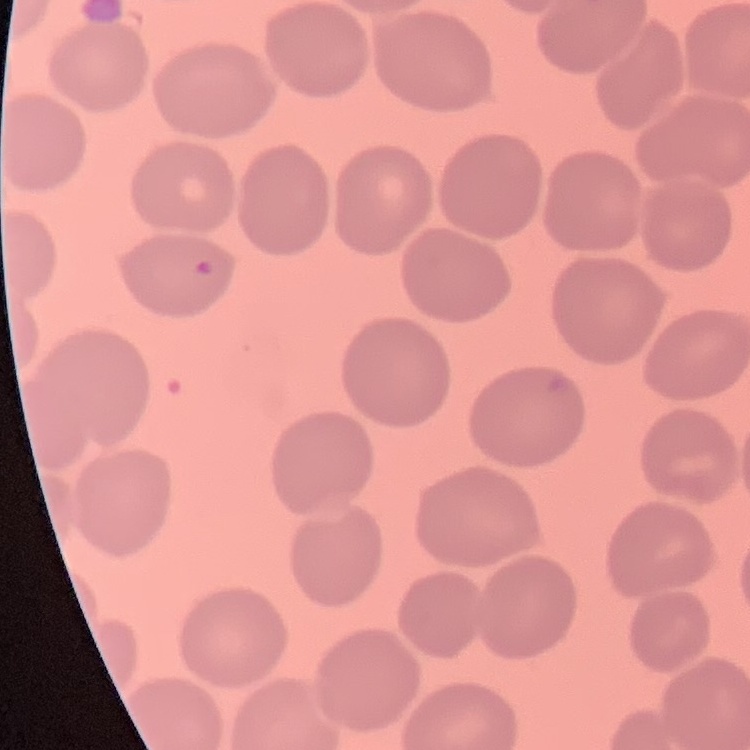
Summary:
  - Erythrocyte morphology: no rouleaux formation
  - Image type: one tile cut from a larger photomicrograph
  - Preparation: thin blood film
  - Stain: Field's or Giemsa